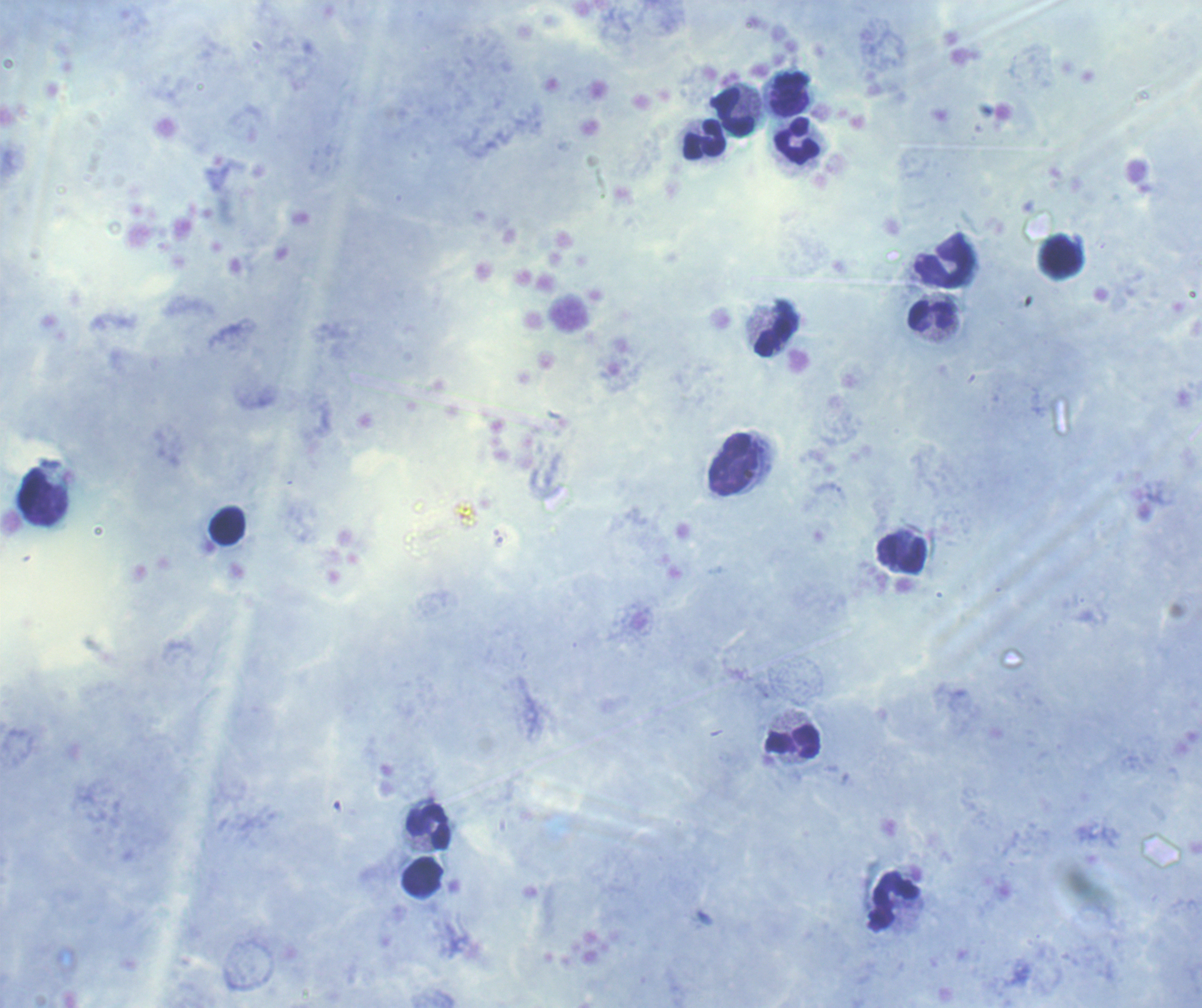 Approximate centers as {x, y} in pixels. Leukocyte locations: {790, 94}, {734, 112}, {704, 139}, {797, 141}, {1060, 256}, {943, 261}, {931, 315}, {772, 336}, {734, 465}, {227, 525}, {902, 554}, {792, 741}, {428, 827}, {423, 877}, {894, 901}. Thick blood smear. Coloration quality: good. Romanowsky-stained preparation. Previously used in a real diagnosis. Result: negative for Plasmodium parasites. Captured at 100x magnification. Background quality: satisfactory. One field from this slide. Image is 1202×1008 pixels.